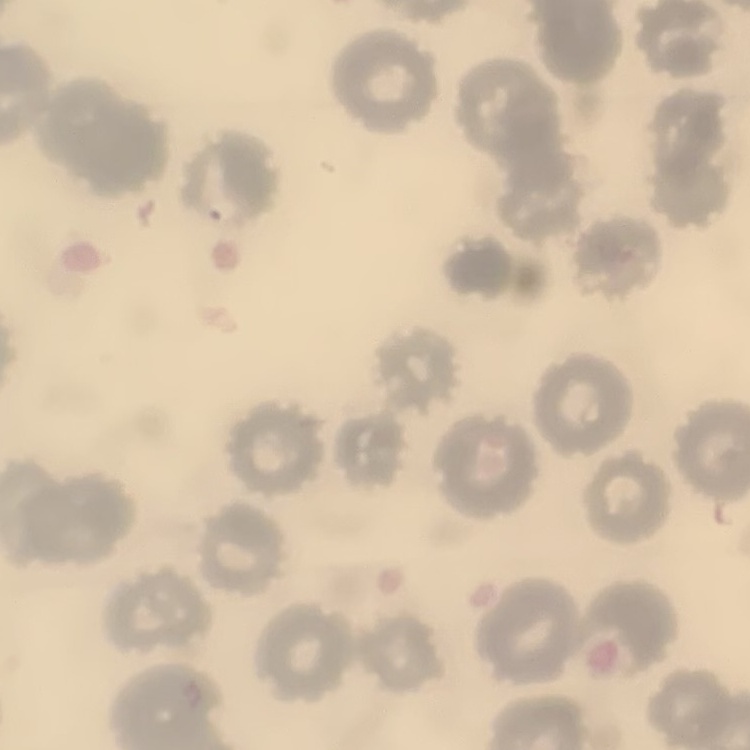 The red blood cells exhibit no rouleaux formation. Thin blood smear. Field's or Giemsa stain. One tile cut from a larger photomicrograph.